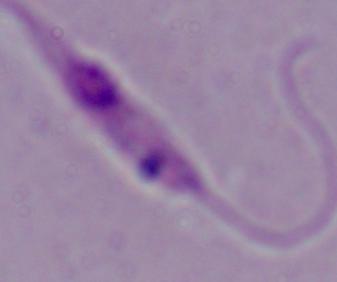

Photomicrograph. A Leishmania parasite is shown. Captured at 1000x magnification.